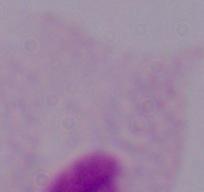
Photomicrograph. A trichomonad is shown. 1000x magnification.